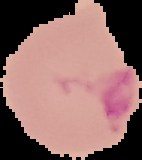

preparation = thin blood film
image type = segmented cell region with the area outside set to black
result = malaria parasites detected
image size = 142×160 pixels